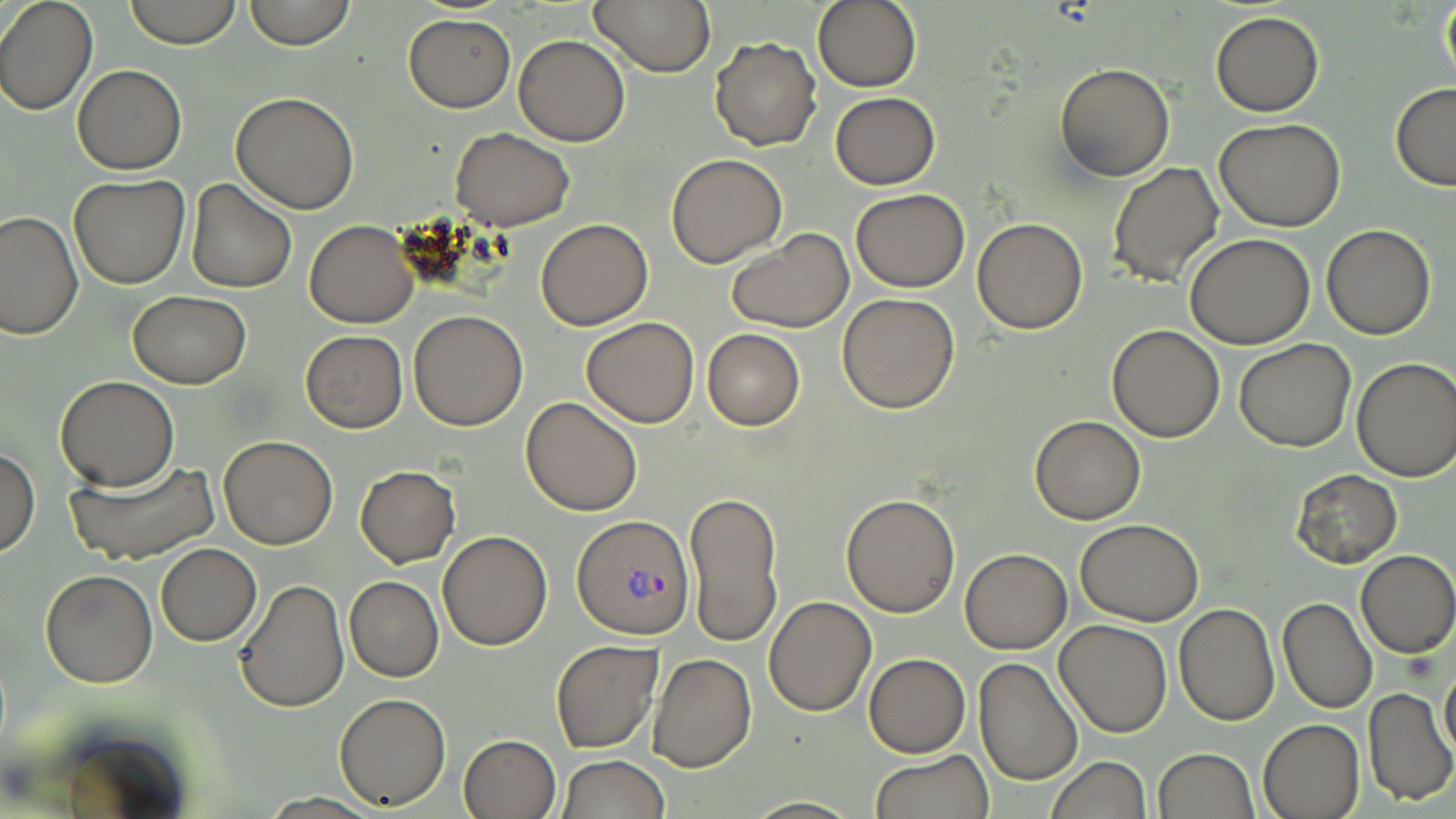
Summary:
  - Coordinate format: approximate bounding boxes as [x1, y1, x2, y2] in pixels
  - Plasmodium vivax-infected red blood cell locations: [573, 514, 695, 638]
  - Uninfected red blood cell locations: [0, 0, 98, 115], [124, 0, 241, 48], [242, 0, 358, 50], [589, 0, 713, 75], [812, 0, 923, 93], [1438, 1, 1456, 98], [1211, 11, 1325, 117], [403, 13, 514, 111], [514, 34, 630, 146], [711, 37, 821, 150], [1054, 62, 1175, 182], [73, 65, 186, 174], [1390, 83, 1456, 192], [231, 91, 359, 213], [831, 92, 940, 189], [1214, 118, 1346, 232], [451, 126, 574, 230], [667, 153, 787, 268], [1108, 161, 1223, 286], [69, 175, 190, 288], [186, 179, 297, 293], [849, 189, 971, 292], [1, 209, 82, 340], [972, 217, 1087, 333], [535, 218, 652, 330], [305, 220, 417, 328], [1322, 223, 1436, 340], [726, 230, 855, 331], [1186, 233, 1314, 349], [130, 291, 252, 388], [838, 292, 961, 413], [408, 309, 528, 430], [580, 317, 701, 428], [1105, 325, 1225, 441], [702, 328, 805, 430], [301, 330, 408, 432], [1234, 340, 1357, 452], [1351, 356, 1456, 481], [56, 377, 180, 490], [520, 396, 643, 516], [1029, 415, 1146, 524], [218, 435, 338, 549], [0, 447, 39, 559], [66, 459, 219, 564], [355, 466, 460, 567], [1292, 470, 1402, 566], [685, 487, 784, 648], [842, 493, 961, 616], [1075, 518, 1204, 624], [439, 530, 552, 650], [156, 544, 262, 646], [960, 547, 1072, 654], [1356, 549, 1455, 658], [41, 570, 158, 689], [345, 576, 444, 682], [233, 578, 350, 713], [764, 595, 876, 716], [1278, 596, 1376, 713], [1174, 604, 1279, 725], [1054, 620, 1172, 737], [550, 639, 663, 753], [647, 652, 756, 773], [864, 653, 971, 758], [973, 657, 1083, 788], [1440, 660, 1456, 762], [1362, 687, 1454, 806], [334, 692, 452, 809], [1259, 718, 1365, 819], [459, 733, 560, 819], [1153, 748, 1259, 819], [870, 751, 993, 819], [558, 755, 671, 818], [1045, 757, 1151, 818], [738, 797, 864, 817]
  - Slide-level diagnosis: Plasmodium vivax
  - Preparation: thin blood smear
  - Modality: optical microscopy
  - Image size: 1456×819 pixels
  - Field of view: single
  - Stain: May-Grünwald-Giemsa
  - Magnification: 1000x